Name the parasite shown.
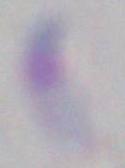

This is Toxoplasma gondii.

Micrograph. 1000x magnification.